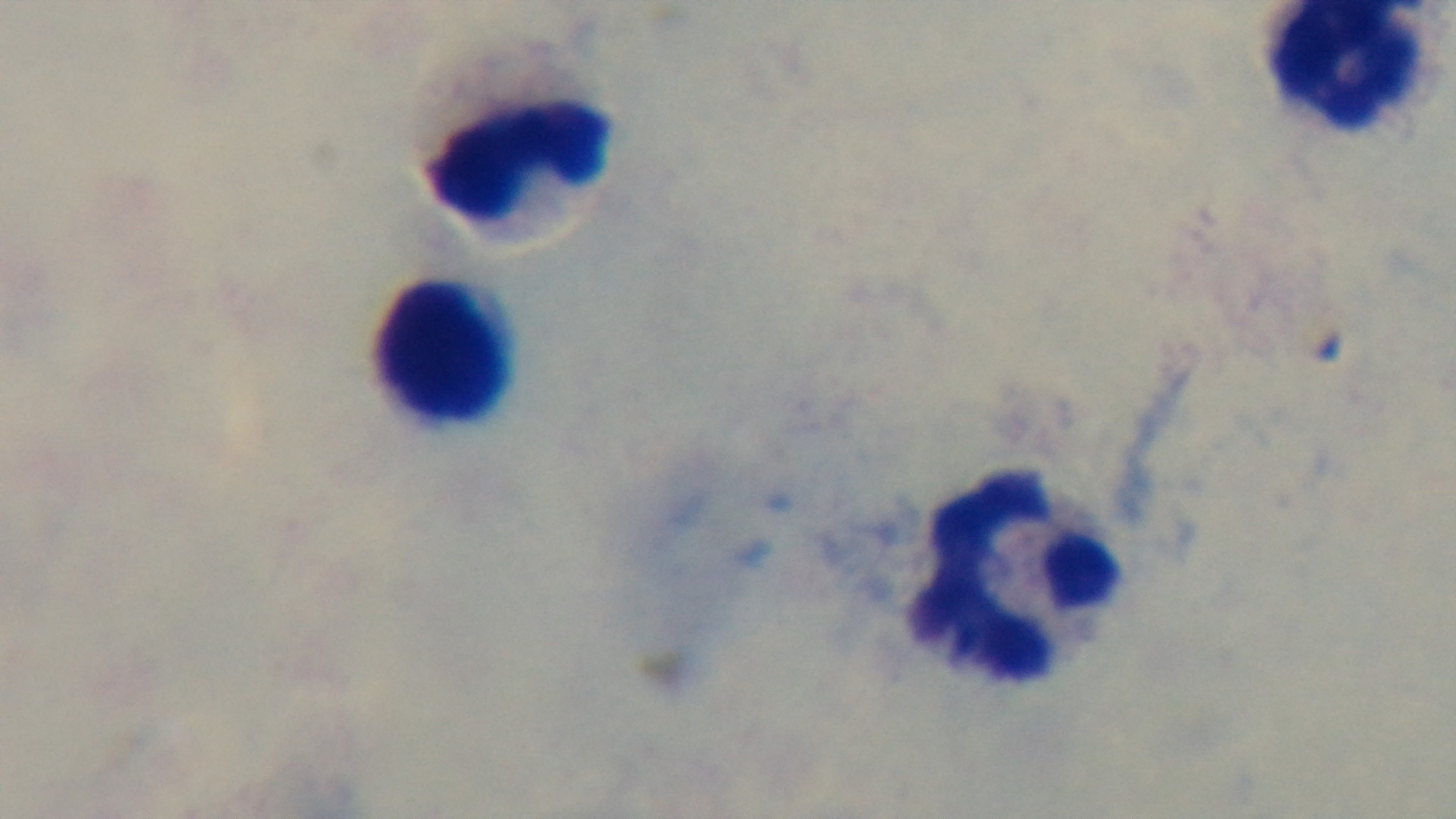
Preparation: thick. Oil-immersion objective, 100x. Captured with a mounted 4K digital camera. Malaria status: negative. Light microscopy. Giemsa-stained. Single field of view.